Identify the preparation type.
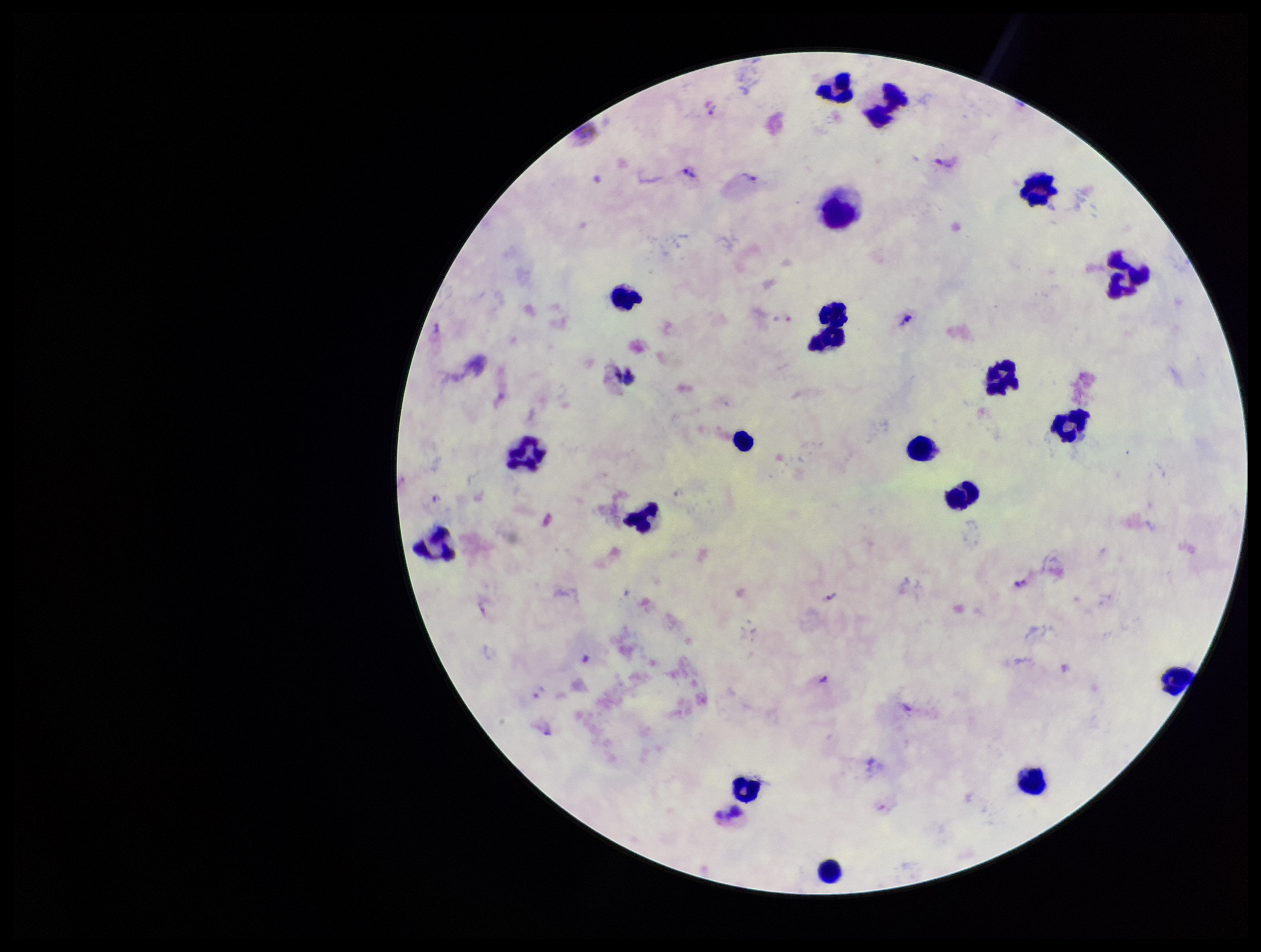

A thick smear.

Giemsa stain. Image is 1261×952 pixels. Smartphone photograph taken through the eyepiece of a microscope. Parasite count: 5. Plasmodium parasites: seen. Leukocyte count: 20. One field from this slide. Species reported for this patient: Plasmodium vivax. Patient malaria status: positive.